State which parasite is depicted.
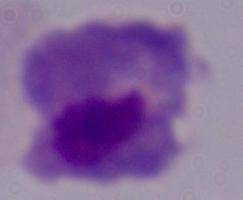
This is a trichomonad.

{
  "magnification": "1000x",
  "modality": "photomicrograph"
}